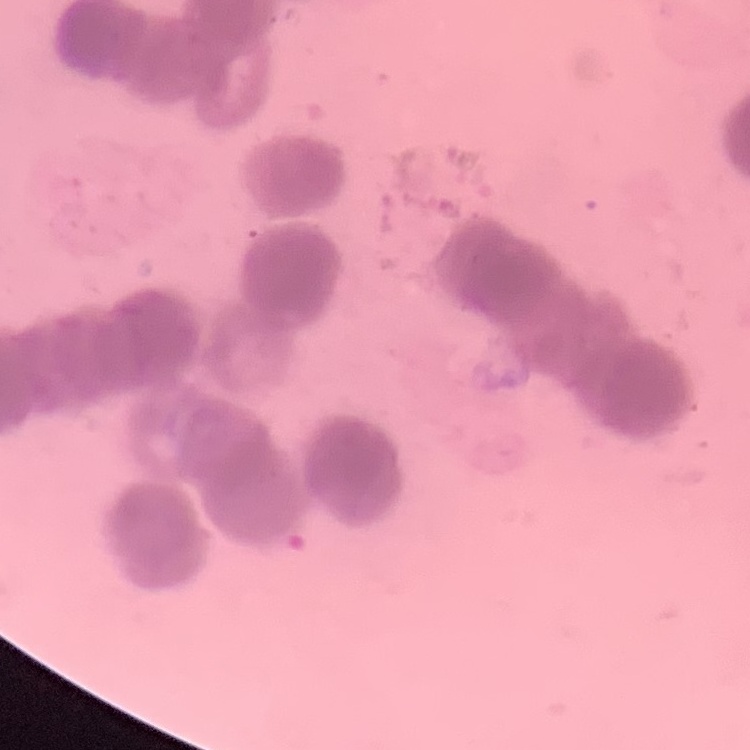

erythrocyte morphology = rouleaux formation
image type = square crop of a larger photomicrograph
stain = Field's or Giemsa
preparation = thin blood film